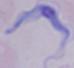
identification = trypanosome
modality = micrograph
magnification = 1000x